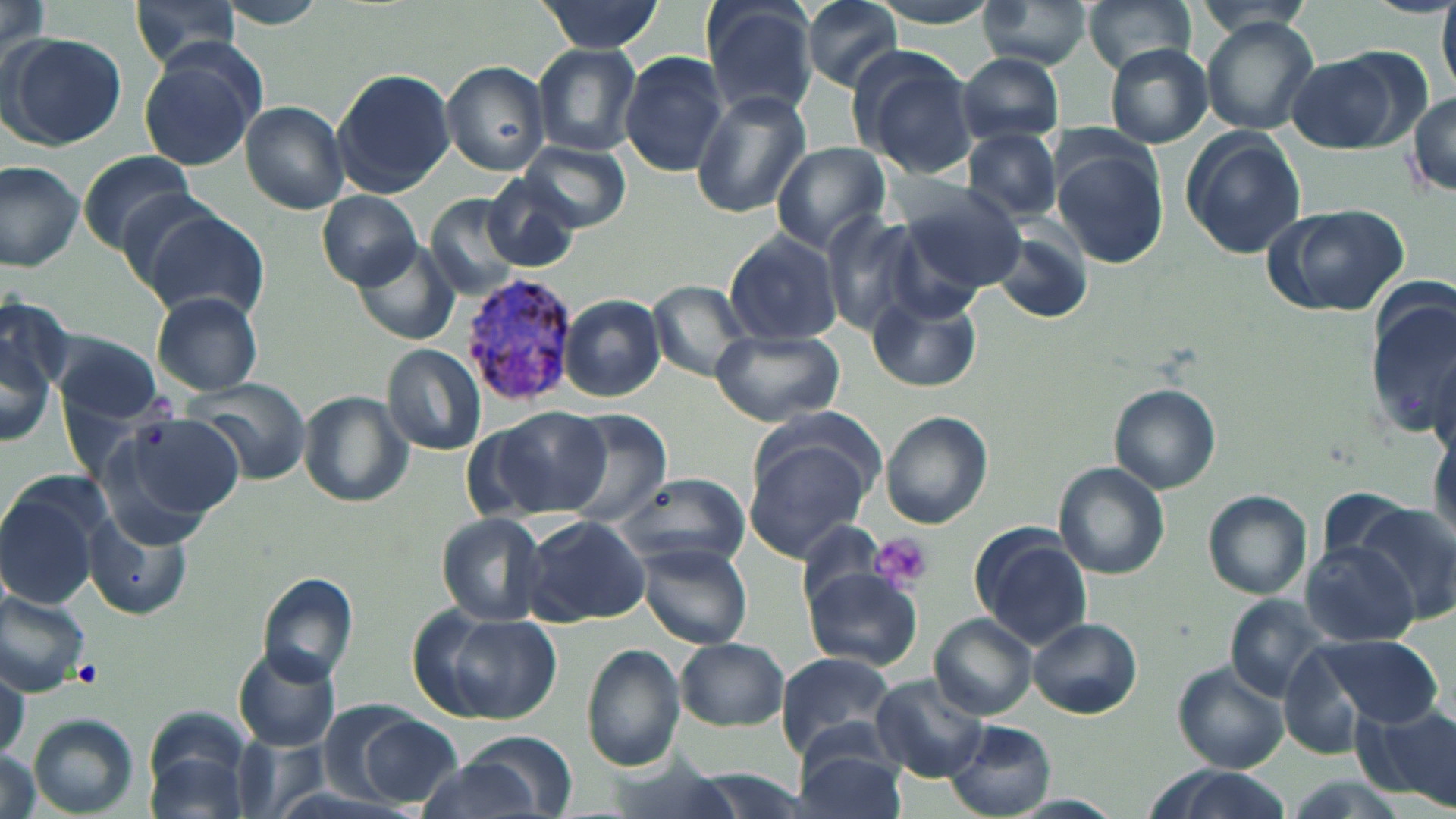
Summary:
  - Coordinate format: approximate bounding boxes as [x1, y1, x2, y2] in pixels
  - Platelet locations: [870, 534, 932, 591], [72, 658, 100, 685]
  - Uninfected red blood cell locations: [1, 0, 50, 65], [125, 0, 245, 71], [804, 0, 904, 91], [975, 0, 1099, 71], [1080, 0, 1198, 74], [701, 1, 819, 119], [1438, 1, 1455, 92], [536, 2, 663, 51], [1203, 18, 1321, 136], [4, 32, 126, 151], [533, 43, 644, 157], [1104, 44, 1213, 146], [138, 45, 263, 173], [846, 45, 977, 179], [1281, 50, 1417, 153], [619, 52, 729, 176], [955, 53, 1067, 146], [444, 62, 551, 176], [333, 67, 453, 195], [1410, 89, 1455, 194], [691, 91, 811, 218], [240, 102, 349, 214], [966, 128, 1064, 220], [1180, 128, 1306, 260], [519, 141, 630, 230], [772, 142, 890, 252], [1051, 146, 1168, 270], [76, 149, 200, 254], [0, 159, 86, 273], [480, 174, 584, 271], [897, 183, 1030, 291], [318, 192, 424, 287], [427, 195, 527, 301], [1264, 203, 1410, 317], [138, 207, 270, 323], [820, 211, 926, 336], [987, 224, 1097, 327], [724, 231, 843, 344], [352, 240, 461, 346], [650, 281, 756, 377], [151, 291, 264, 396], [868, 291, 982, 393], [1, 293, 73, 400], [560, 295, 665, 401], [1365, 295, 1453, 438], [0, 320, 56, 451], [52, 331, 165, 425], [709, 331, 844, 426], [383, 344, 486, 456], [185, 377, 314, 485], [1109, 383, 1220, 493], [299, 390, 413, 507], [489, 403, 613, 518], [111, 410, 247, 527], [553, 410, 671, 527], [880, 411, 992, 529], [741, 435, 877, 561], [1054, 462, 1170, 579], [611, 473, 751, 568], [0, 477, 109, 612], [1203, 489, 1312, 600], [1342, 499, 1456, 628], [435, 512, 551, 626], [84, 514, 187, 620], [521, 516, 652, 626], [799, 520, 891, 610], [969, 523, 1094, 647], [1301, 541, 1421, 648], [637, 543, 753, 650], [803, 569, 923, 670], [258, 574, 358, 687], [0, 583, 94, 698], [1227, 594, 1336, 700], [410, 606, 561, 725], [930, 616, 1038, 720], [1027, 617, 1143, 720], [1309, 634, 1444, 728], [675, 637, 789, 731], [581, 643, 685, 772], [233, 647, 339, 752], [775, 651, 904, 765], [1172, 662, 1289, 772], [0, 666, 28, 758], [871, 676, 988, 782], [1359, 702, 1456, 809], [143, 710, 257, 819], [27, 714, 139, 816], [357, 716, 463, 804], [945, 722, 1057, 817], [464, 732, 578, 814], [793, 734, 909, 819], [0, 746, 49, 819], [414, 758, 547, 819], [1132, 767, 1301, 819]
  - Plasmodium vivax-infected red blood cell locations: [461, 272, 583, 409]
  - Slide-level diagnosis: Plasmodium vivax
  - Image size: 1456×819 pixels
  - Preparation: thin blood smear
  - Stain: May-Grünwald-Giemsa
  - Magnification: 1000x
  - Modality: optical microscopy
  - Field of view: one of a larger specimen